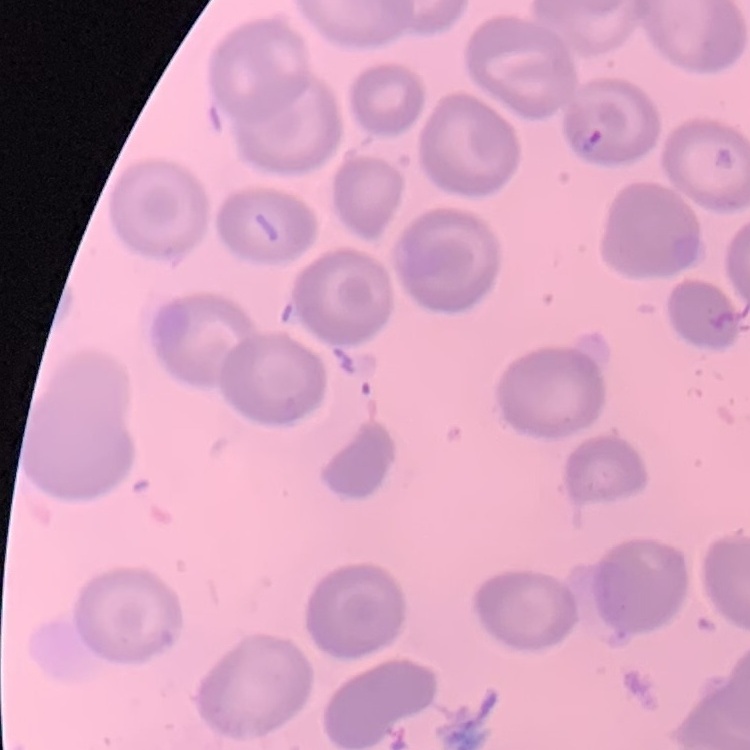
{
  "red_blood_cell_morphology": "no rouleaux formation",
  "preparation": "thin peripheral smear",
  "image_type": "one tile cut from a larger photomicrograph",
  "stain": "Field's or Giemsa"
}